Name the parasite shown.
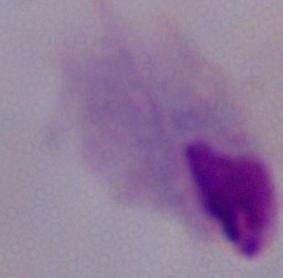
A trichomonad.

Micrograph. 1000x magnification.